Report the malaria status of this cell.
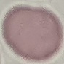

It is uninfected.

Automatically extracted cell patch, resized to 64 × 64 pixels. Giemsa stain. Thin blood smear. Photographed with a smartphone camera at the microscope eyepiece.